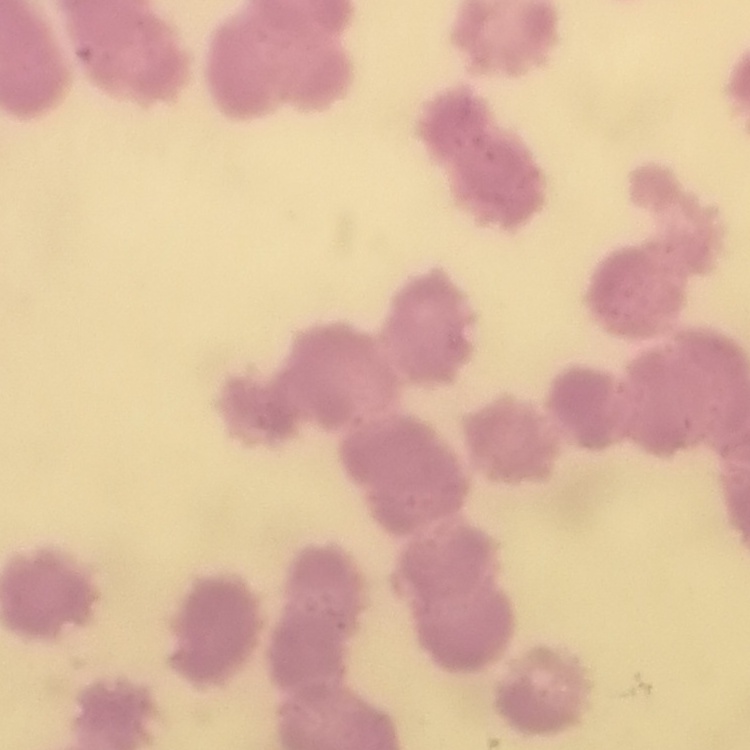

Summary:
  - Red blood cell morphology: rouleaux formation
  - Image type: square crop of a larger photomicrograph
  - Preparation: thin blood film
  - Stain: Field's or Giemsa